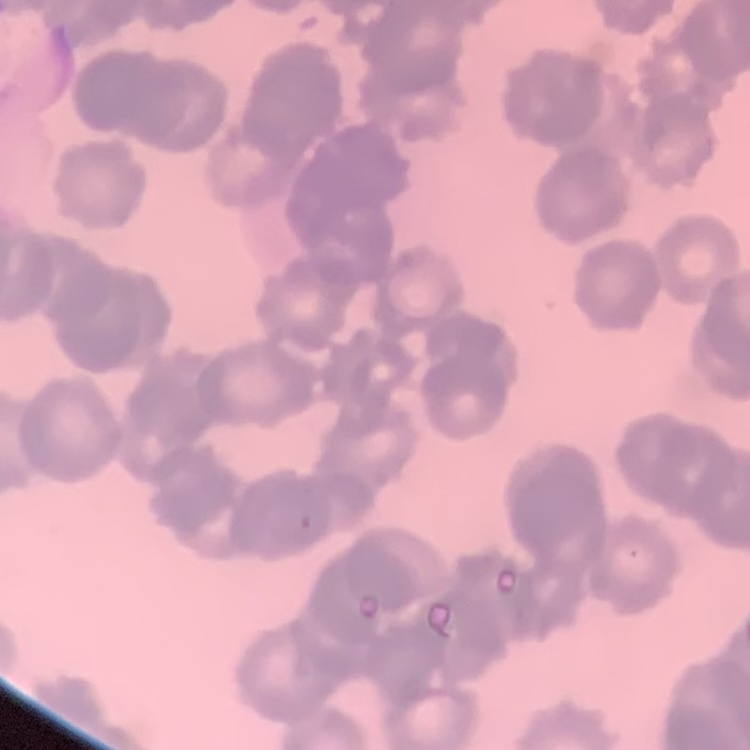

Summary:
  - Red blood cell morphology: rouleaux formation
  - Preparation: thin peripheral smear
  - Image type: one tile cut from a larger photomicrograph
  - Stain: Field's or Giemsa